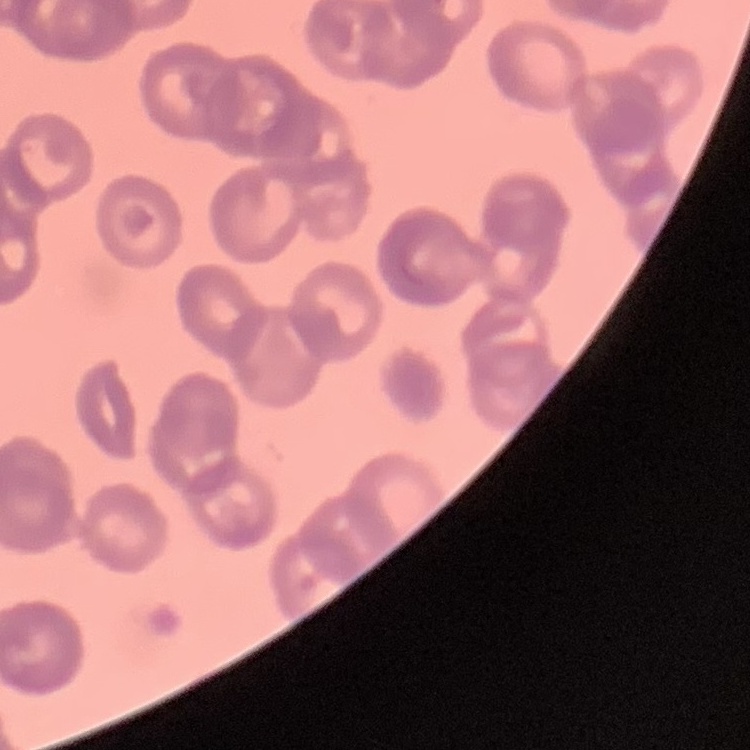
The erythrocytes exhibit rouleaux formation. Field's or Giemsa stain. Square crop of a larger photomicrograph. Thin blood smear.